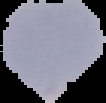

From a thin blood smear. Cell region segmented out of the field of view; the surrounding area is masked to black. Result: no Plasmodium parasites seen. Image is 106×103 pixels.